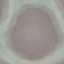
Malaria status: uninfected. Photographed with a smartphone camera at the microscope eyepiece. Giemsa-stained preparation. Cell patch, automatically extracted from a larger field of view and resized to 64 × 64 pixels. Thin smear of blood.